Locate every blood parasite and identify its species.
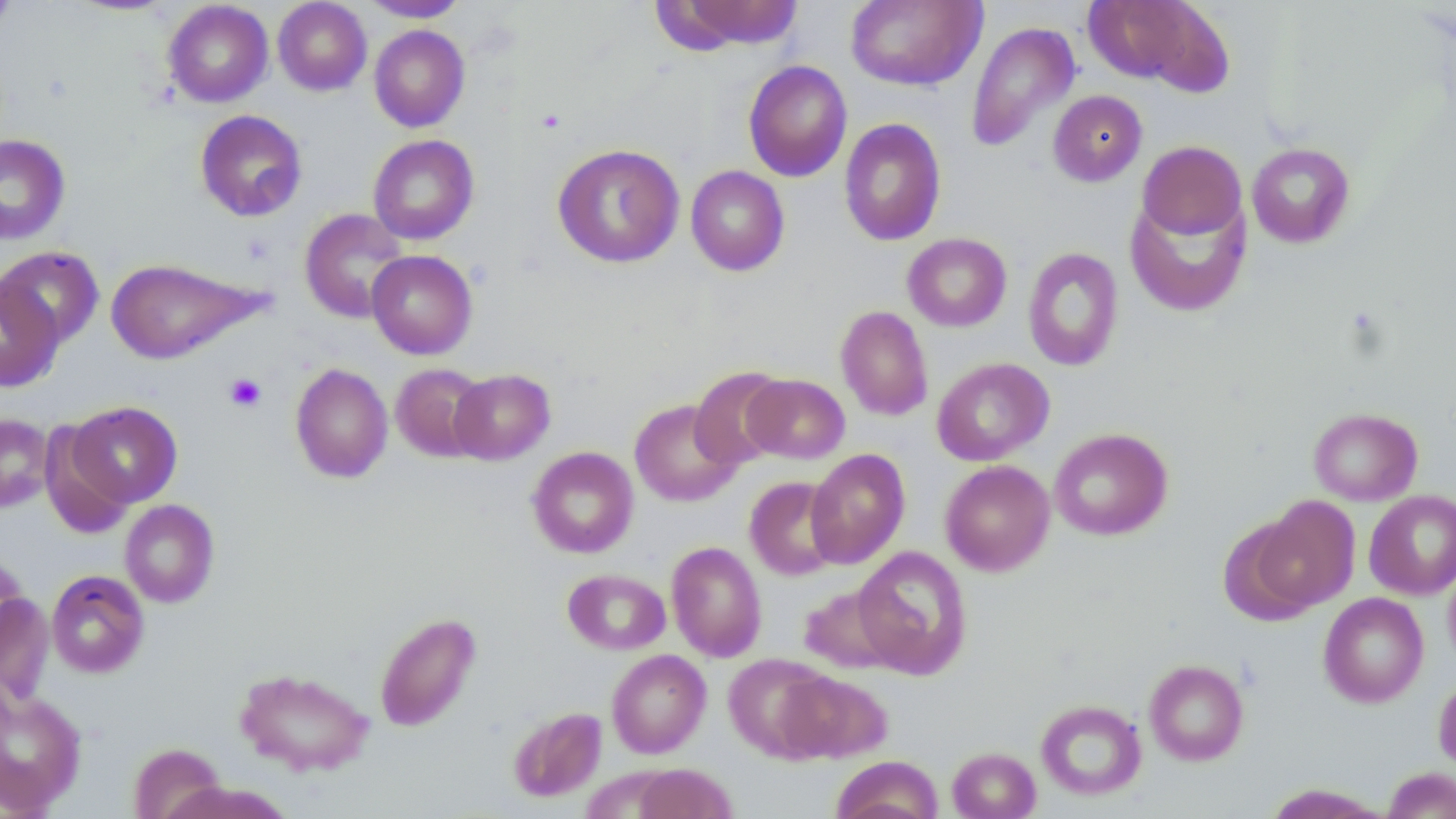

No blood parasites observed.

Approximate bounding boxes as (x1,y1)-(x2,y2) corner pairs in pixels. Platelet locations: (224,373)-(267,412). Uninfected red blood cell locations: (0,0)-(16,33), (67,0)-(179,16), (273,0)-(372,96), (360,0)-(470,22), (845,0)-(985,91), (163,1)-(273,107), (672,1)-(804,49), (1084,2)-(1219,89), (965,20)-(1081,154), (369,25)-(470,132), (743,60)-(852,182), (1048,90)-(1147,187), (195,109)-(307,222), (839,118)-(947,246), (0,134)-(71,244), (368,134)-(479,245), (1137,141)-(1246,240), (1246,142)-(1356,248), (552,143)-(684,268), (685,165)-(790,276), (1125,193)-(1251,317), (299,208)-(410,323), (902,233)-(1012,332), (0,245)-(104,348), (1023,247)-(1124,372), (367,250)-(477,359), (106,258)-(260,364), (0,277)-(64,392), (835,305)-(933,421), (931,357)-(1055,466), (290,362)-(393,483), (391,363)-(491,462), (689,367)-(790,468), (448,369)-(555,465), (743,373)-(850,463), (629,399)-(743,507), (67,401)-(182,507), (1308,408)-(1423,505), (0,414)-(54,512), (39,422)-(135,539), (1049,428)-(1173,541), (526,446)-(639,558), (805,448)-(910,569), (940,460)-(1055,576), (744,476)-(845,580), (1364,490)-(1456,599), (1249,497)-(1360,614), (120,499)-(219,608), (666,541)-(767,662), (852,545)-(973,679), (1443,561)-(1456,673), (562,568)-(670,655), (46,570)-(149,677), (799,583)-(900,673), (1,591)-(54,706), (1318,592)-(1429,707), (373,611)-(482,732), (607,650)-(711,758), (725,653)-(837,760), (1144,659)-(1249,765), (235,667)-(375,776), (777,670)-(893,763), (1433,676)-(1456,774), (0,689)-(86,814), (1035,699)-(1146,800), (508,706)-(607,802), (129,743)-(226,819), (947,747)-(1041,819), (830,755)-(943,819), (633,763)-(737,819), (1383,767)-(1456,818), (165,781)-(295,819), (1263,784)-(1390,818). Slide-level diagnosis: no evidence of blood parasites. Image is 1456×819 pixels. Light microscopy. May-Grünwald-Giemsa-stained preparation. 1000x magnification. Thin blood film. Single field of view.